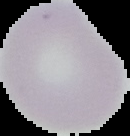

image_type: segmented cell region with the area outside set to black
malaria_status: uninfected
image_size: 130×136 pixels
preparation: thin blood film